Classify this cell by malaria status.
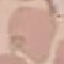
Uninfected.

Cell patch, automatically extracted from a larger field of view and resized to 64 × 64 pixels. Photographed with a smartphone camera at the microscope eyepiece. Thin blood smear. Giemsa-stained preparation.